Assess the morphology of the red blood cells.
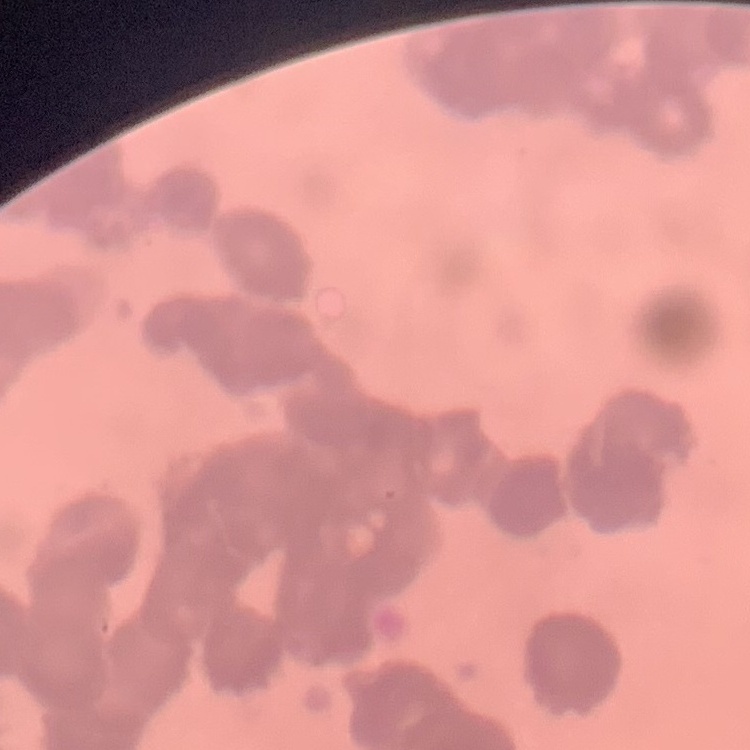

Rouleaux formation.

{
  "preparation": "thin peripheral smear",
  "stain": "Field's or Giemsa",
  "image_type": "one tile cut from a larger photomicrograph"
}